State which cell type is depicted.
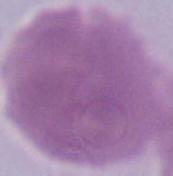
This is an erythrocyte.

modality = micrograph
magnification = 1000x